Report the malaria status of this cell.
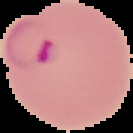

It is parasitized.

image type = segmented cell region with the area outside set to black
image size = 133×133 pixels
preparation = thin blood smear